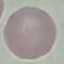

malaria status = uninfected
stain = Giemsa
capture = smartphone through the microscope eyepiece
image type = automatically extracted cell patch, resized to 64 × 64 pixels
preparation = thin blood film